Classify this cell by malaria status.
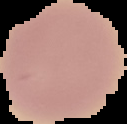

It is uninfected.

Summary:
  - Image size: 127×124 pixels
  - Preparation: thin blood film
  - Image type: segmented cell region on a black background